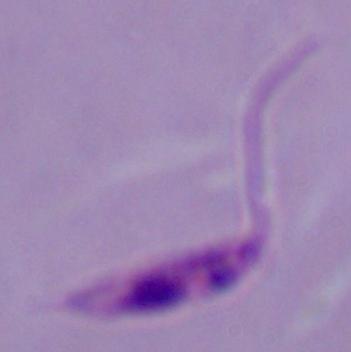
Summary:
  - Magnification: 1000x
  - Modality: photomicrograph
  - Identification: Leishmania